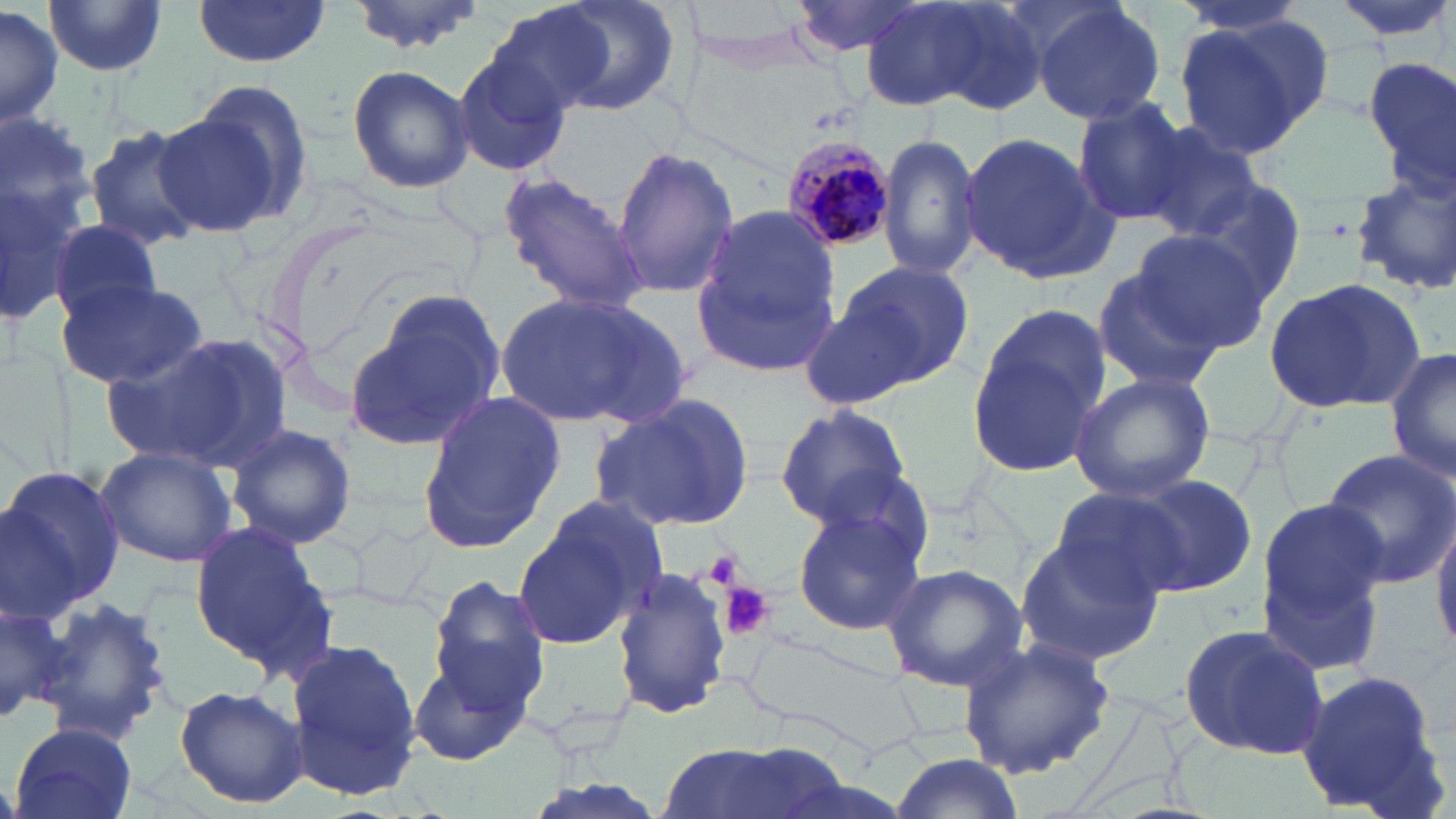

Approximate bounding boxes as [x1, y1, x2, y2] in pixels. Uninfected red blood cell locations: [528, 0, 682, 119], [788, 0, 931, 57], [857, 0, 1010, 113], [1330, 0, 1456, 41], [345, 1, 485, 55], [681, 1, 825, 69], [43, 2, 168, 77], [190, 2, 331, 67], [925, 2, 1051, 115], [1028, 2, 1167, 128], [0, 5, 61, 127], [483, 6, 613, 123], [1170, 15, 1328, 158], [452, 47, 576, 178], [1363, 57, 1456, 180], [344, 64, 475, 195], [156, 93, 306, 238], [1071, 100, 1194, 224], [0, 122, 99, 323], [82, 124, 209, 251], [1137, 124, 1265, 241], [958, 132, 1115, 283], [878, 133, 981, 282], [612, 147, 739, 297], [1350, 165, 1456, 294], [497, 172, 650, 313], [1179, 175, 1306, 314], [688, 205, 846, 378], [50, 218, 165, 328], [1134, 229, 1276, 353], [822, 257, 975, 393], [1092, 264, 1228, 391], [1262, 278, 1425, 417], [60, 280, 207, 388], [348, 291, 509, 453], [495, 293, 690, 429], [793, 293, 919, 407], [967, 307, 1109, 477], [104, 332, 286, 471], [1385, 348, 1456, 485], [1069, 372, 1216, 502], [415, 391, 566, 557], [589, 391, 758, 532], [775, 405, 912, 525], [224, 423, 357, 551], [95, 445, 236, 569], [1320, 446, 1456, 588], [0, 464, 125, 617], [808, 466, 940, 581], [1116, 472, 1257, 598], [1049, 486, 1187, 602], [519, 498, 665, 647], [792, 498, 928, 639], [1254, 499, 1391, 660], [1432, 512, 1456, 655], [188, 519, 336, 681], [1012, 534, 1164, 668], [878, 563, 1029, 689], [610, 568, 733, 723], [426, 574, 551, 725], [0, 590, 70, 731], [32, 593, 172, 746], [1176, 623, 1331, 760], [734, 625, 924, 752], [287, 637, 425, 802], [956, 637, 1116, 779], [406, 650, 533, 767], [1294, 667, 1447, 814], [174, 684, 307, 809], [10, 723, 139, 819], [650, 739, 850, 819], [893, 753, 1023, 818]. Platelet locations: [698, 549, 747, 591], [720, 581, 773, 641]. Plasmodium malariae-infected red blood cell locations: [777, 134, 895, 256]. Slide-level diagnosis: Plasmodium malariae. Single field of view. Image is 1456×819 pixels. Thin blood film. 1000x magnification. Optical microscopy. May-Grünwald-Giemsa stain.